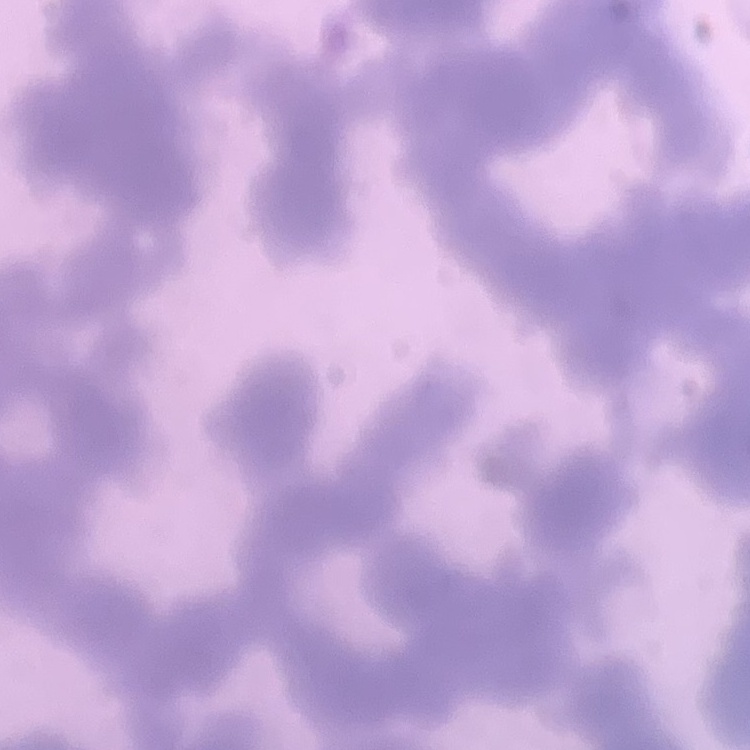 The red blood cells exhibit rouleaux formation. Field's or Giemsa stain. Thin peripheral smear. One tile cut from a larger photomicrograph.